Assess for malaria.
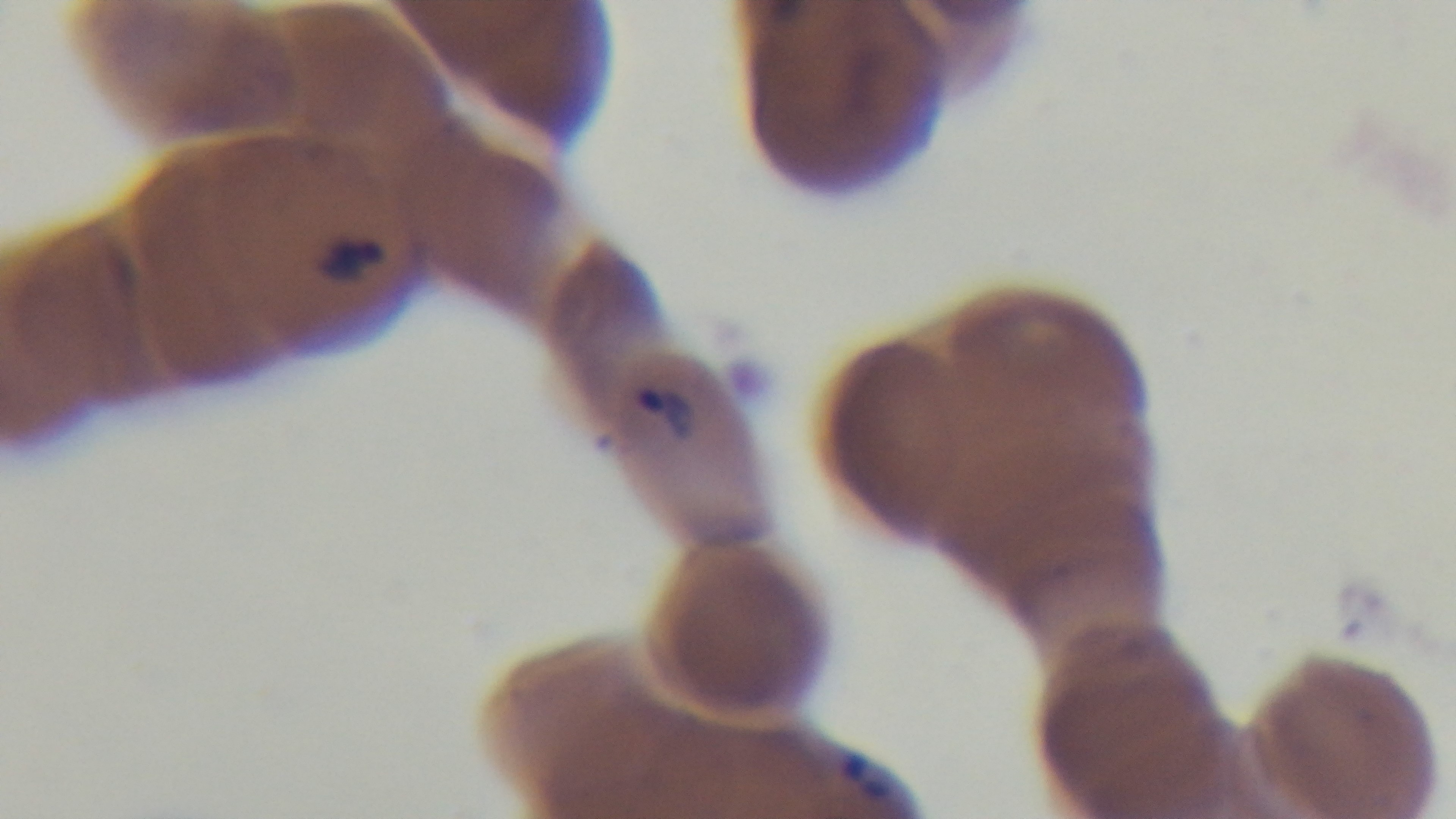
Infected.

{
  "capture": "mounted 4K digital camera",
  "objective": "100x oil immersion",
  "modality": "light microscopy",
  "preparation": "thin",
  "field_of_view": "one from the slide",
  "stain": "Giemsa"
}